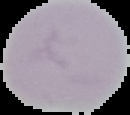
Summary:
  - Preparation: thin blood film
  - Image type: segmented cell region with the area outside set to black
  - Result: negative for Plasmodium parasites
  - Image size: 130×115 pixels